Assess this cell for malaria.
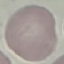
Uninfected.

image type = cell patch, automatically extracted from a larger field of view and resized to 64 × 64 pixels
capture = smartphone camera at the microscope eyepiece
stain = Giemsa
preparation = thin smear